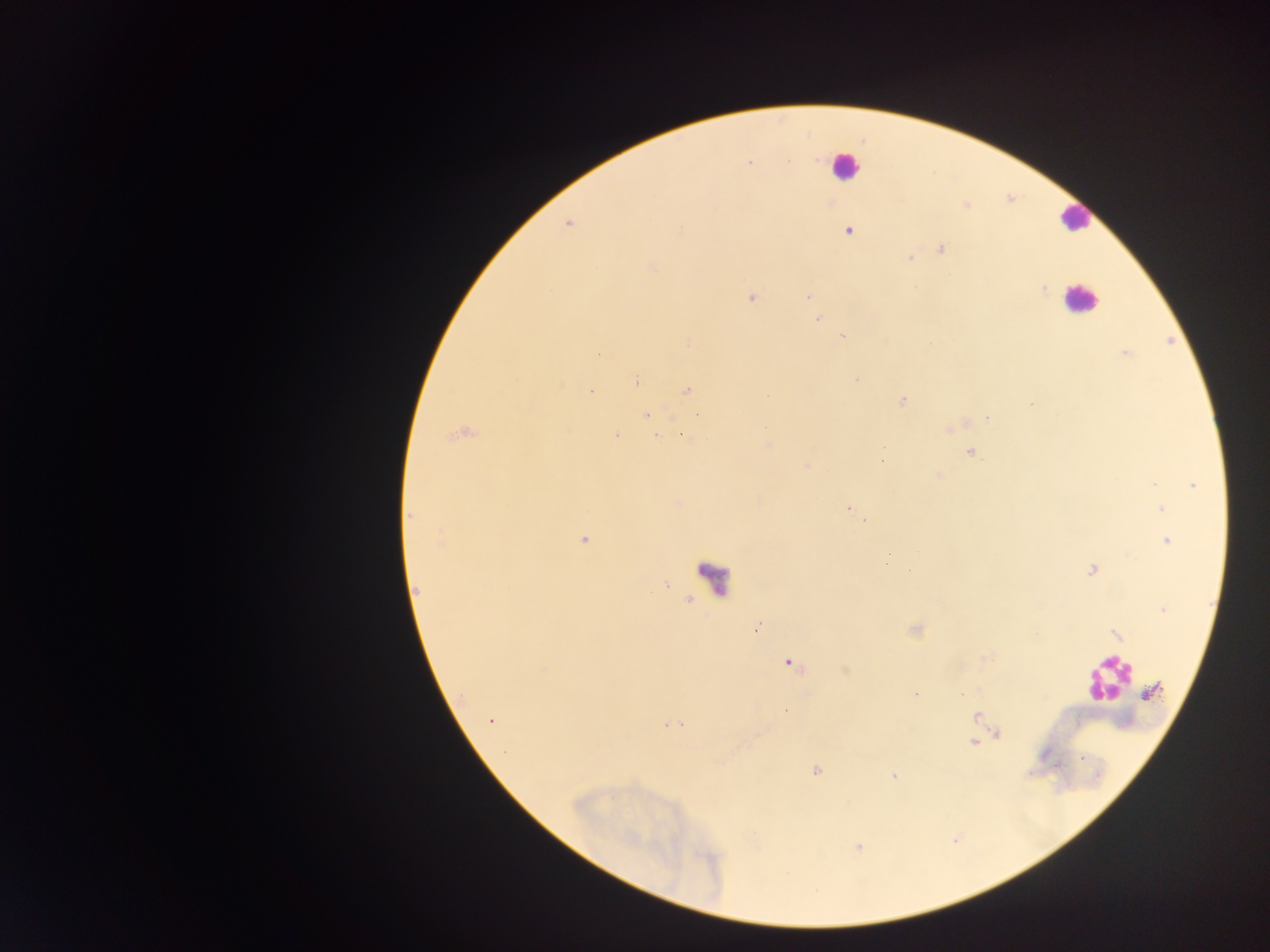
leukocyte locations = approximate centers as (x, y) in pixels: (843, 165), (1074, 220), (1081, 302), (1104, 682)
field of view = single
country = Ghana
preparation = thick blood smear
image size = 1270×952 pixels
capture = mobile-phone photograph through a microscope
malaria parasite locations = approximate centers as (x, y) in pixels: (831, 202), (680, 230), (849, 230), (941, 249), (909, 257), (652, 266), (1043, 288), (806, 295), (751, 296), (818, 318), (843, 338), (688, 343), (1124, 354), (855, 379), (636, 381), (687, 389), (592, 390), (901, 402), (1031, 403), (645, 415), (695, 415), (988, 417), (766, 425), (948, 429), (678, 431), (459, 434), (615, 434), (681, 435), (654, 437), (768, 445), (882, 447), (971, 451), (883, 452), (883, 460), (805, 465), (938, 475), (1195, 485), (848, 507), (1161, 509), (412, 517), (865, 520), (583, 540), (1167, 540), (888, 554), (910, 568), (1091, 570), (664, 584), (415, 589), (1164, 609), (757, 627), (914, 629), (1116, 635), (787, 662), (845, 668), (915, 693), (786, 709), (490, 719), (667, 725), (997, 733), (973, 741), (816, 770), (894, 774), (858, 848)